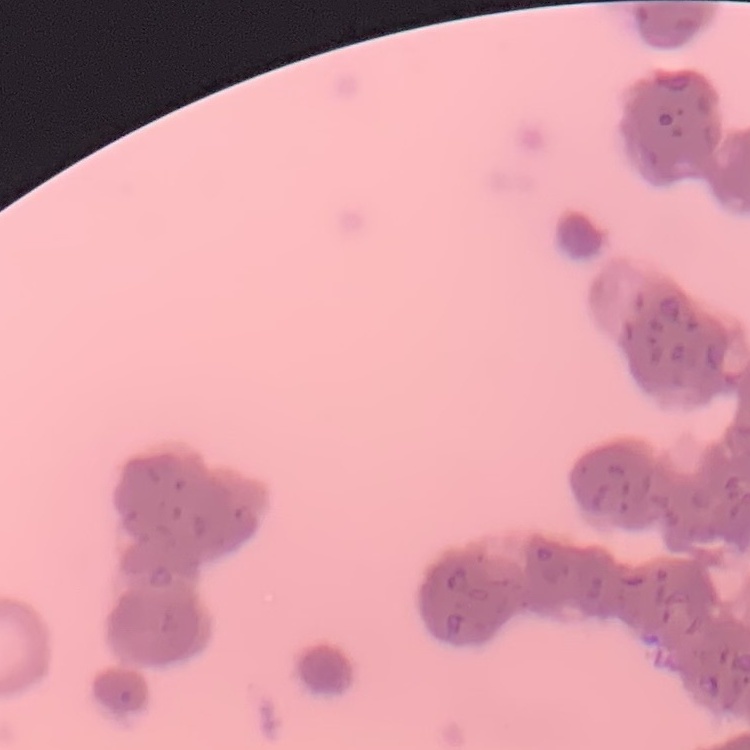

erythrocyte_morphology: rouleaux formation
preparation: thin blood film
image_type: square crop of a larger photomicrograph
stain: Field's or Giemsa